Name the parasite shown.
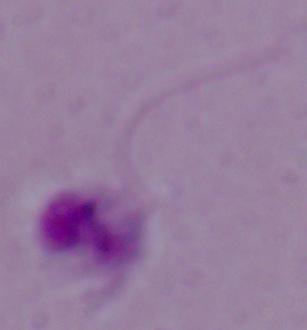

This is Leishmania.

Micrograph. Captured at 1000x magnification.